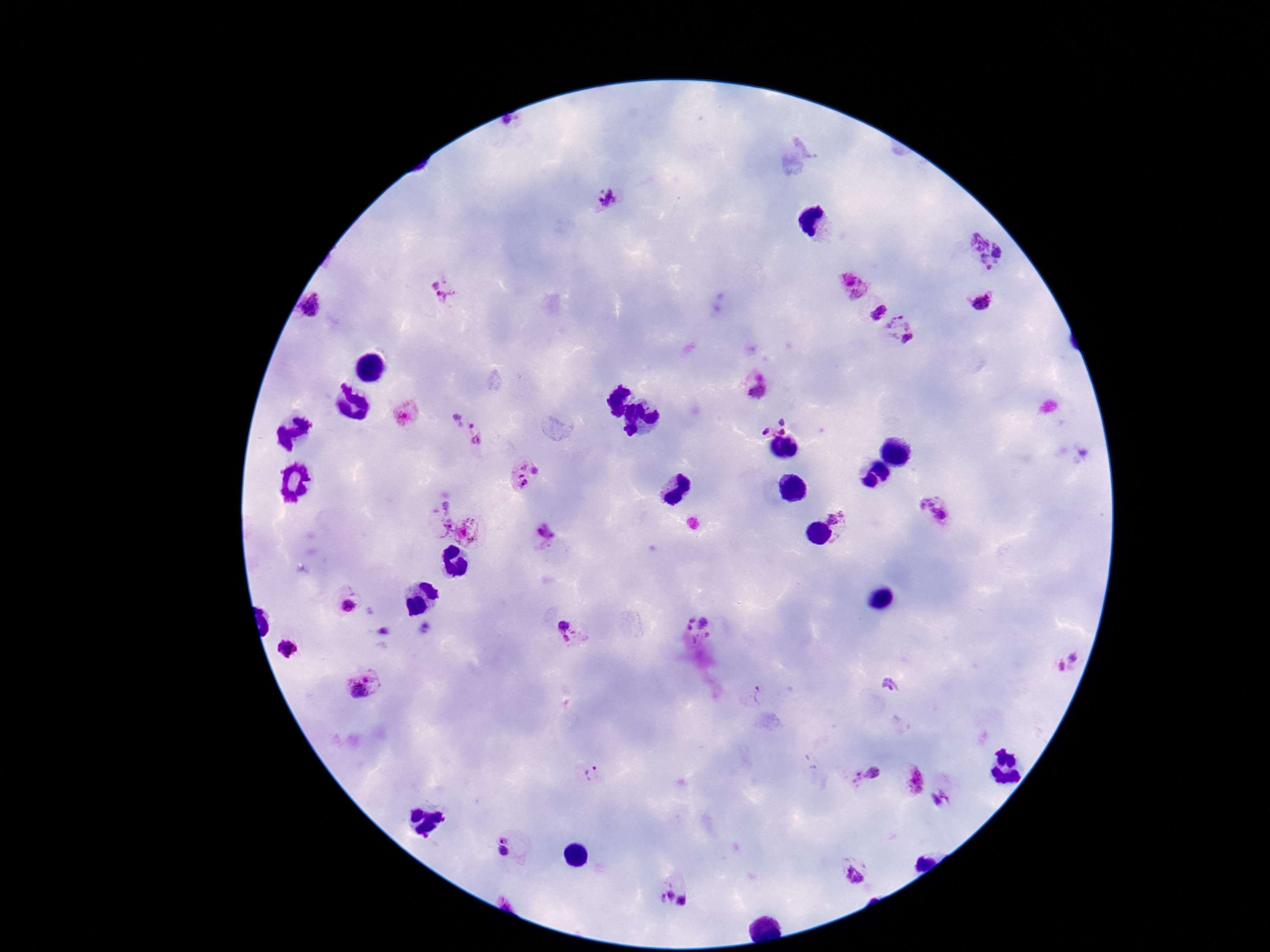
Approximate centers as (x, y) in pixels.
Summary:
  - Plasmodium parasite locations: (608, 198), (987, 252), (853, 284), (446, 292), (984, 304), (311, 307), (879, 311), (899, 332), (757, 388), (408, 417), (776, 418), (466, 432), (526, 478), (935, 513), (833, 515), (435, 520), (470, 532), (543, 536), (344, 606), (564, 630), (699, 631), (284, 648), (1066, 663), (362, 686), (760, 695), (592, 774), (863, 774), (911, 781), (942, 800), (502, 835), (504, 850), (854, 876), (664, 895), (682, 902)
  - Magnification: 100x
  - Capture: smartphone camera through the microscope eyepiece
  - Preparation: thick peripheral-blood smear
  - Stain: Giemsa
  - Image size: 1270×952 pixels
  - Patient malaria status: positive
  - Field of view: single